Identify the blood parasite species.
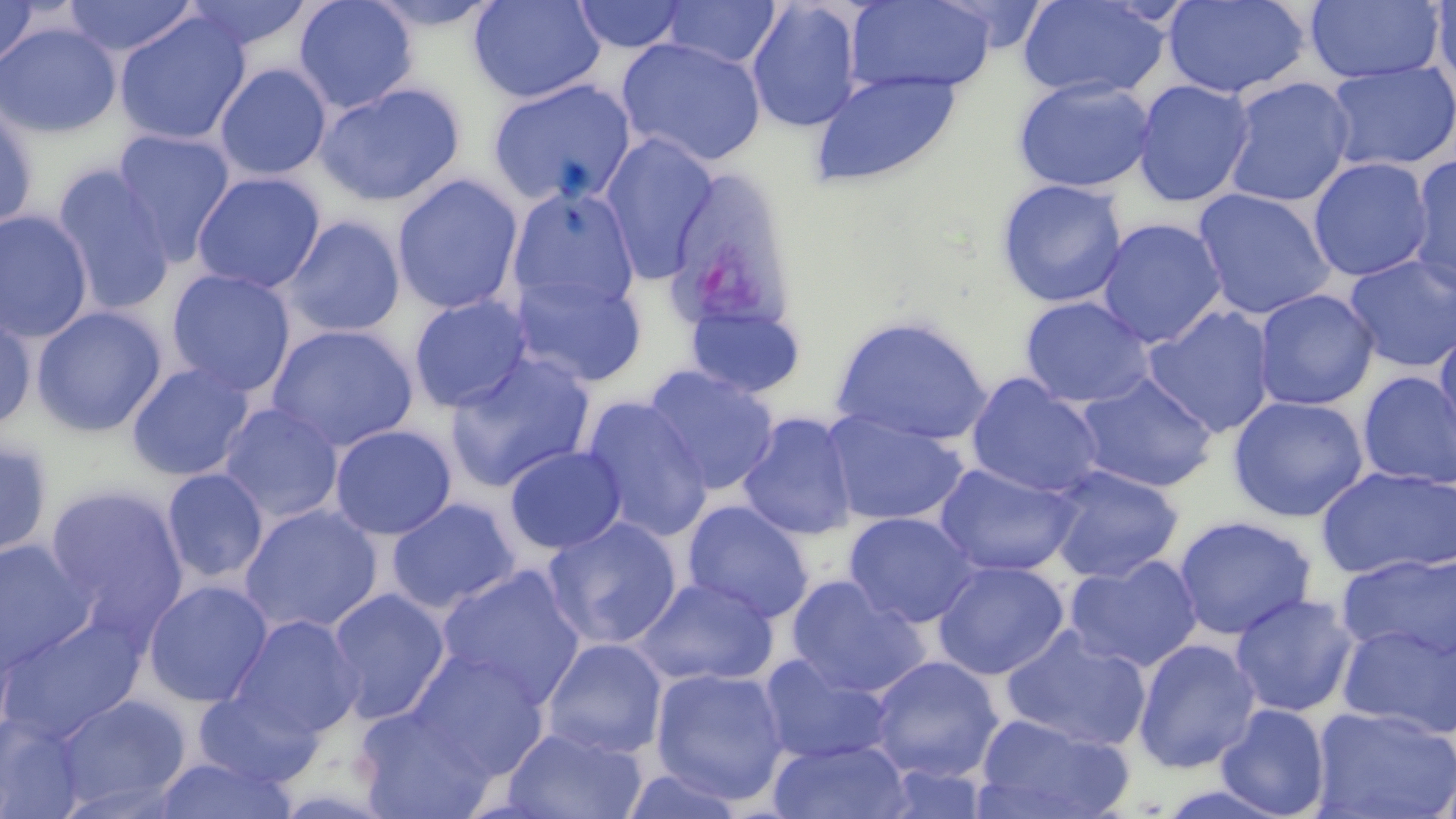
Plasmodium vivax.

Summary:
  - Coordinate format: approximate bounding boxes as (x1, y1, x2, y2) in pixels
  - Plasmodium vivax-infected red blood cell locations: (662, 169, 798, 337)
  - Uninfected red blood cell locations: (61, 0, 199, 58), (181, 0, 315, 54), (293, 0, 419, 114), (361, 0, 506, 32), (468, 0, 606, 104), (745, 0, 864, 133), (845, 0, 998, 95), (1017, 0, 1171, 101), (1430, 0, 1456, 96), (570, 1, 690, 54), (659, 1, 783, 69), (1164, 1, 1309, 99), (1306, 1, 1446, 84), (0, 3, 38, 70), (113, 11, 251, 147), (0, 22, 121, 139), (616, 37, 767, 168), (1324, 61, 1456, 173), (214, 63, 332, 181), (809, 70, 961, 189), (1013, 76, 1157, 193), (1222, 77, 1355, 207), (486, 78, 637, 206), (1132, 79, 1255, 207), (314, 81, 466, 207), (0, 103, 38, 234), (110, 128, 237, 266), (599, 132, 720, 282), (1406, 153, 1456, 296), (1308, 157, 1433, 282), (50, 164, 177, 317), (191, 171, 326, 294), (392, 174, 524, 314), (996, 178, 1128, 308), (506, 185, 640, 313), (1193, 187, 1336, 320), (0, 210, 95, 343), (283, 216, 406, 338), (1096, 218, 1228, 348), (1344, 254, 1456, 373), (166, 268, 297, 397), (510, 270, 648, 387), (1253, 289, 1380, 411), (408, 294, 533, 413), (1020, 296, 1155, 408), (682, 297, 808, 399), (1143, 304, 1277, 438), (30, 305, 167, 438), (0, 308, 37, 433), (830, 314, 994, 446), (266, 324, 418, 452), (1434, 329, 1456, 463), (444, 352, 597, 492), (125, 362, 255, 482), (643, 364, 780, 495), (1358, 371, 1456, 490), (1074, 372, 1218, 493), (965, 373, 1106, 499), (580, 395, 714, 542), (1228, 395, 1369, 522), (218, 402, 344, 523), (821, 410, 970, 526), (737, 412, 860, 541), (329, 424, 457, 540), (0, 437, 54, 561), (504, 445, 627, 555), (934, 462, 1082, 578), (1046, 464, 1184, 583), (1315, 466, 1456, 581), (160, 468, 269, 585), (43, 482, 189, 638), (387, 497, 522, 613), (681, 500, 815, 623), (239, 503, 384, 635), (843, 511, 980, 628), (1172, 515, 1317, 641), (542, 516, 683, 650), (0, 539, 95, 676), (1336, 552, 1456, 664), (1064, 554, 1204, 673), (932, 559, 1070, 680), (436, 564, 586, 709), (785, 575, 930, 698), (632, 576, 778, 688), (142, 580, 273, 707), (326, 587, 450, 723), (1230, 593, 1360, 717), (0, 613, 147, 744), (229, 614, 363, 740), (1336, 621, 1456, 740), (1000, 624, 1153, 752), (540, 637, 667, 759), (1132, 638, 1262, 774), (405, 649, 549, 778), (758, 653, 895, 765), (868, 655, 1004, 782), (650, 666, 790, 805), (193, 688, 324, 788), (52, 692, 192, 813), (1215, 704, 1331, 819), (1310, 705, 1456, 819), (354, 706, 497, 819), (0, 712, 88, 817), (972, 713, 1133, 819), (502, 725, 648, 819), (769, 738, 912, 819), (150, 754, 299, 818)
  - Image size: 1456×819 pixels
  - Preparation: thin blood smear
  - Stain: May-Grünwald-Giemsa
  - Modality: light microscopy
  - Field of view: single
  - Magnification: 1000x